Locate every blood parasite and identify its species.
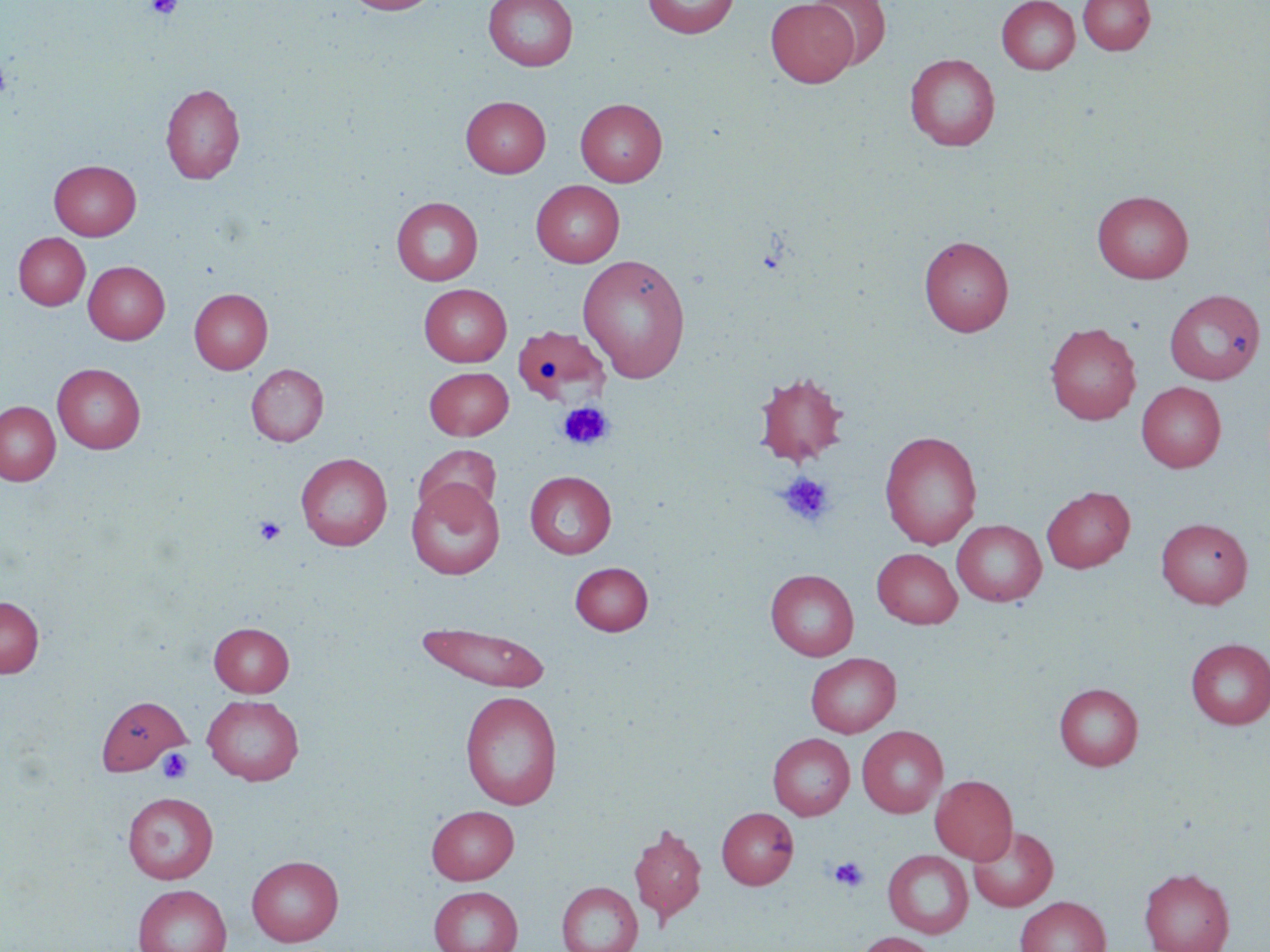

No blood parasites seen.

Approximate bounding boxes as [x1, y1, x2, y2] in pixels. Platelet locations: [146, 0, 183, 20], [0, 56, 13, 102], [557, 401, 614, 451], [777, 472, 834, 527], [254, 516, 287, 545], [158, 747, 193, 783], [829, 856, 869, 893]. Uninfected red blood cell locations: [342, 0, 440, 15], [484, 0, 578, 71], [643, 0, 740, 39], [809, 0, 891, 69], [996, 0, 1080, 74], [1078, 0, 1155, 55], [765, 1, 859, 87], [905, 54, 1000, 151], [160, 82, 245, 183], [461, 95, 550, 177], [575, 98, 667, 186], [49, 160, 141, 240], [531, 180, 624, 267], [1092, 190, 1194, 283], [391, 197, 483, 285], [13, 232, 90, 310], [919, 236, 1014, 336], [577, 254, 691, 383], [83, 260, 170, 344], [419, 283, 512, 366], [189, 288, 273, 374], [1164, 288, 1266, 385], [1045, 322, 1141, 425], [514, 328, 613, 412], [52, 363, 145, 453], [246, 364, 328, 446], [424, 366, 513, 440], [753, 371, 849, 467], [1136, 381, 1226, 472], [0, 401, 60, 485], [879, 430, 982, 549], [413, 444, 502, 523], [296, 452, 392, 550], [525, 471, 617, 558], [407, 481, 505, 579], [1041, 486, 1136, 573], [1156, 517, 1253, 608], [951, 519, 1046, 606], [872, 548, 962, 628], [570, 562, 653, 635], [766, 569, 859, 661], [0, 596, 44, 677], [209, 622, 294, 697], [416, 622, 552, 692], [1185, 638, 1270, 729], [806, 653, 901, 737], [1054, 682, 1143, 770], [460, 690, 562, 810], [97, 695, 191, 775], [202, 695, 304, 785], [857, 725, 948, 818], [767, 733, 855, 820], [930, 774, 1018, 864], [122, 791, 218, 883], [427, 805, 519, 884], [716, 806, 799, 889], [628, 823, 707, 925], [967, 825, 1058, 912], [882, 849, 973, 938], [247, 855, 343, 946], [1139, 867, 1235, 952], [557, 881, 643, 952], [133, 884, 232, 952], [428, 885, 523, 952], [1015, 896, 1111, 952], [851, 932, 940, 952]. Slide-level diagnosis: negative for blood parasites. One field of a larger specimen. Captured at 1000x magnification. Light microscopy. Thin blood film. Image is 1270×952 pixels. May-Grünwald-Giemsa stain.